State which parasite is depicted.
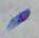

This is Toxoplasma gondii.

Summary:
  - Magnification: 1000x
  - Modality: micrograph